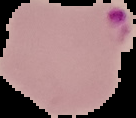

Summary:
  - Preparation: thin blood film
  - Image type: cell region segmented out of the field of view; surrounding area masked to black
  - Result: Plasmodium parasites identified
  - Image size: 136×118 pixels